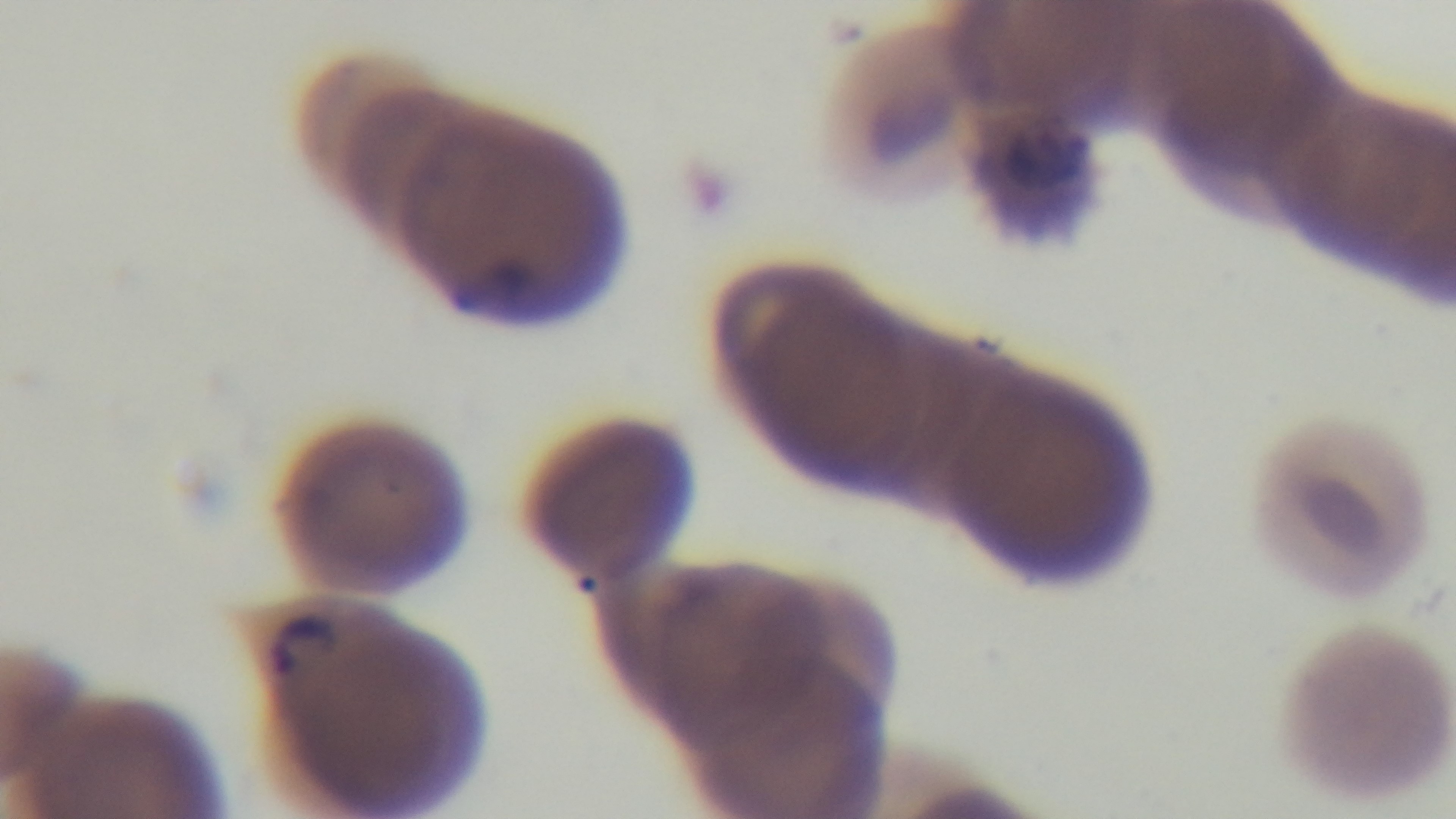
100x oil-immersion objective. Preparation: thin smear. Single field of view. Photomicrograph. Giemsa stain. Mounted 4K digital camera. Malaria status: positive.